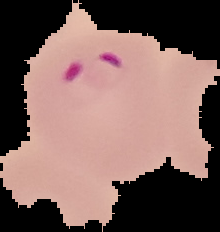
{
  "image_type": "cell region segmented out of the field of view; surrounding area masked to black",
  "image_size": "220×232 pixels",
  "preparation": "thin blood smear",
  "result": "Plasmodium parasites detected"
}